State which parasite is depicted.
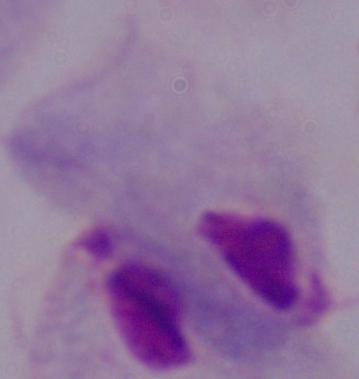

This is a trichomonad.

Summary:
  - Modality: photomicrograph
  - Magnification: 1000x